Assess this cell for malaria.
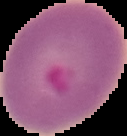
Parasitized.

From a thin blood smear. Image is 127×136 pixels. Segmented cell region on a black background.